State which cell type is depicted.
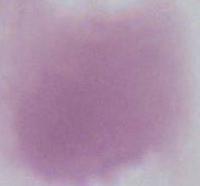

This is an erythrocyte.

Captured at 1000x magnification. Micrograph.